Classify this cell by malaria status.
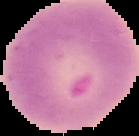

It is uninfected.

Image is 139×136 pixels. Cell region segmented out of the field of view; the surrounding area is masked to black. From a thin blood smear.